Locate every Plasmodium parasite.
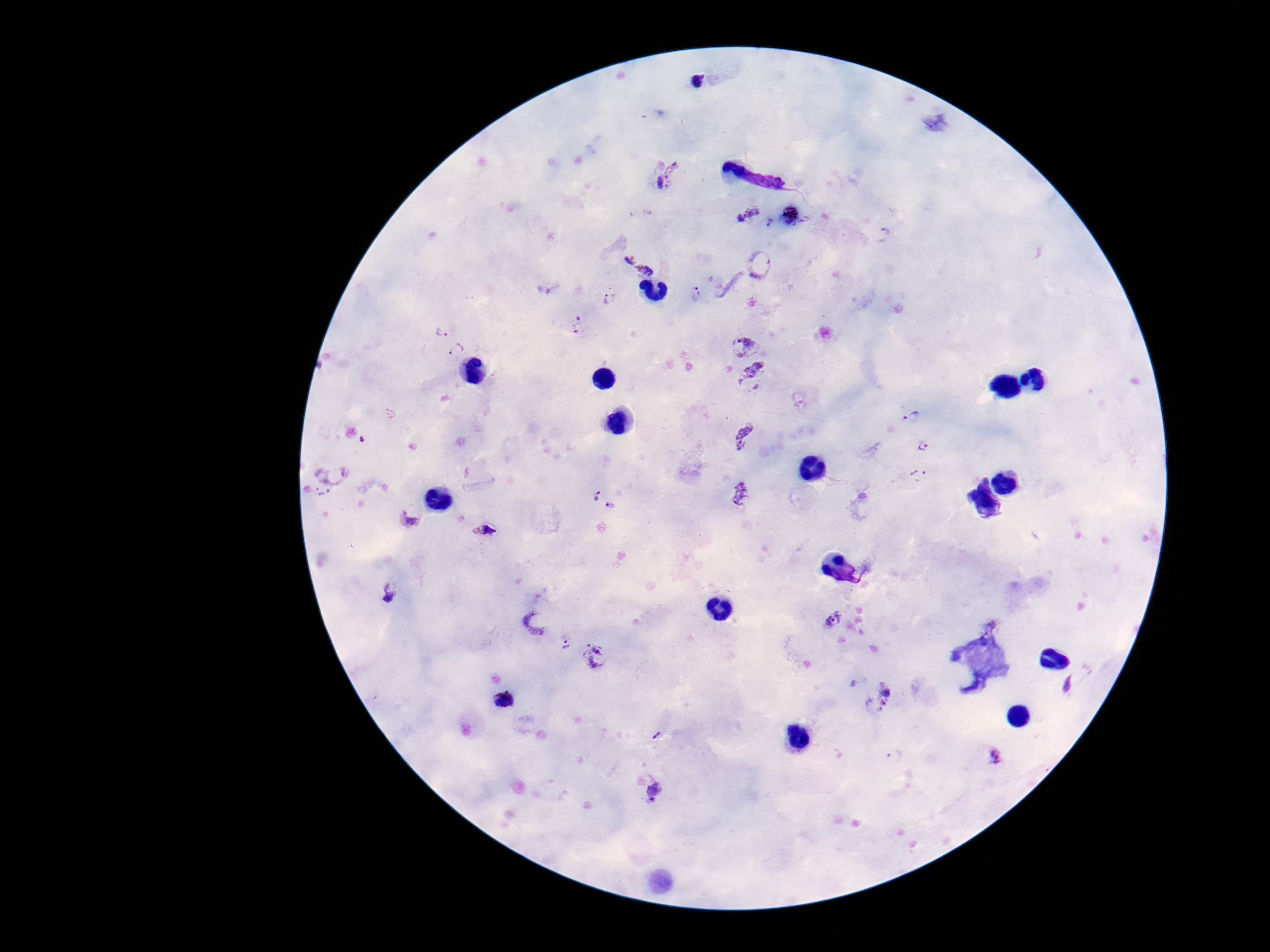
Approximate centers as (x, y) in pixels.
Plasmodium parasites: (695, 80), (669, 178), (749, 213), (881, 235), (628, 256), (761, 263), (647, 269), (698, 294), (611, 298), (439, 325), (576, 325), (742, 343), (457, 350), (756, 371), (914, 416), (743, 433), (364, 440), (925, 447), (334, 468), (918, 474), (594, 494), (741, 496), (322, 497), (612, 508), (410, 518), (487, 529), (389, 589), (535, 620), (832, 621), (566, 643), (597, 656), (1067, 685), (878, 695), (505, 700), (657, 735), (995, 757), (655, 786).

100x magnification. Giemsa-stained preparation. Single field of view. Patient malaria status: positive. Thick blood film. Photographed through the microscope eyepiece with a smartphone camera. Image is 1270×952 pixels.